State the blood parasite species.
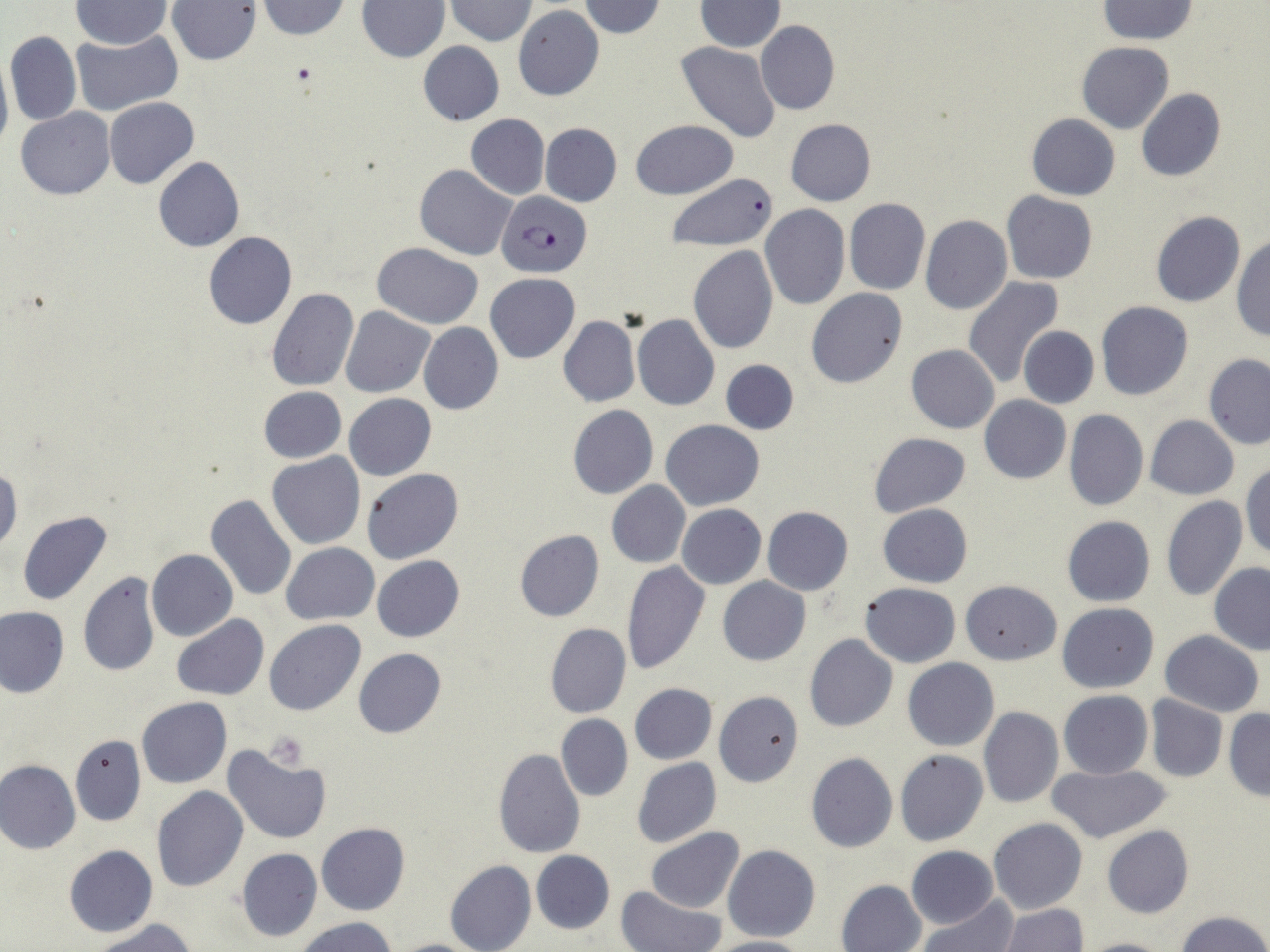

Plasmodium falciparum.

Approximate bounding boxes as [x1, y1, x2, y2] in pixels. Plasmodium falciparum-infected red blood cell locations: [497, 191, 593, 278]. Platelet locations: [262, 731, 309, 769]. Uninfected red blood cell locations: [258, 0, 351, 39], [444, 0, 540, 45], [578, 0, 667, 37], [1097, 0, 1197, 43], [71, 1, 173, 50], [166, 1, 262, 66], [696, 1, 784, 51], [357, 2, 449, 62], [514, 4, 604, 100], [756, 19, 839, 115], [4, 30, 82, 126], [70, 31, 182, 117], [417, 41, 505, 125], [675, 41, 782, 144], [1076, 42, 1174, 134], [0, 50, 13, 160], [1136, 88, 1227, 181], [104, 97, 200, 189], [17, 108, 114, 200], [466, 113, 550, 199], [1027, 114, 1119, 200], [785, 118, 876, 205], [631, 119, 738, 199], [540, 122, 622, 206], [153, 157, 245, 252], [414, 164, 516, 260], [666, 171, 778, 252], [1000, 191, 1097, 283], [844, 198, 931, 296], [759, 205, 851, 311], [1151, 211, 1245, 308], [919, 216, 1012, 315], [202, 231, 296, 330], [1231, 237, 1269, 342], [373, 242, 483, 328], [687, 246, 779, 354], [485, 273, 581, 363], [962, 277, 1064, 388], [266, 288, 359, 391], [806, 288, 907, 389], [1095, 300, 1194, 400], [341, 307, 436, 398], [633, 315, 720, 410], [558, 316, 640, 407], [419, 322, 503, 415], [1018, 326, 1099, 409], [906, 344, 999, 434], [1203, 354, 1270, 449], [721, 359, 798, 436], [258, 386, 347, 463], [344, 394, 436, 480], [979, 396, 1070, 484], [568, 404, 658, 498], [1064, 409, 1147, 512], [1145, 415, 1239, 500], [661, 420, 763, 510], [867, 433, 972, 516], [267, 453, 364, 550], [1242, 463, 1270, 561], [0, 466, 22, 559], [361, 469, 464, 565], [607, 481, 691, 568], [204, 494, 296, 601], [1161, 495, 1247, 602], [877, 503, 972, 588], [677, 504, 766, 589], [762, 507, 853, 595], [17, 510, 113, 606], [1061, 516, 1156, 607], [514, 529, 605, 622], [281, 543, 378, 624], [147, 550, 238, 641], [372, 555, 465, 641], [620, 560, 711, 676], [1209, 563, 1270, 654], [77, 572, 161, 678], [717, 576, 810, 666], [961, 580, 1062, 664], [859, 581, 962, 668], [1056, 602, 1160, 693], [0, 607, 70, 698], [171, 615, 268, 699], [264, 620, 366, 716], [545, 623, 631, 718], [1159, 630, 1265, 717], [804, 634, 898, 733], [353, 648, 447, 739], [902, 657, 999, 751], [629, 684, 717, 764], [711, 689, 805, 787], [1058, 690, 1154, 779], [1145, 695, 1227, 782], [137, 697, 233, 788], [979, 706, 1063, 808], [1223, 709, 1270, 800], [556, 714, 632, 802], [72, 735, 145, 826], [222, 745, 332, 844], [491, 748, 586, 859], [894, 749, 988, 846], [805, 752, 898, 853], [632, 756, 722, 847], [1, 759, 81, 855], [175, 762, 305, 871], [1047, 763, 1174, 845], [152, 786, 248, 890], [988, 817, 1088, 915], [316, 823, 410, 915], [1103, 824, 1193, 918], [645, 827, 744, 913], [64, 844, 158, 937], [722, 844, 821, 943], [906, 845, 999, 929], [235, 847, 323, 943], [531, 849, 615, 934], [445, 859, 537, 952], [836, 878, 927, 952], [617, 886, 727, 952], [918, 896, 1017, 952], [998, 904, 1088, 952], [1174, 910, 1270, 952], [296, 917, 398, 952], [92, 919, 197, 952], [701, 936, 811, 952], [1079, 937, 1173, 952], [389, 938, 487, 952]. 1000x magnification. Image is 1270×952 pixels. Single field of view. Optical microscopy. Thin blood film. May-Grünwald-Giemsa stain.